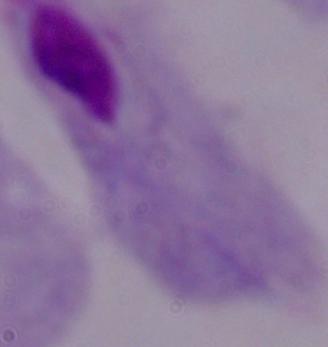

Summary:
  - Magnification: 1000x
  - Identification: trichomonad
  - Modality: micrograph